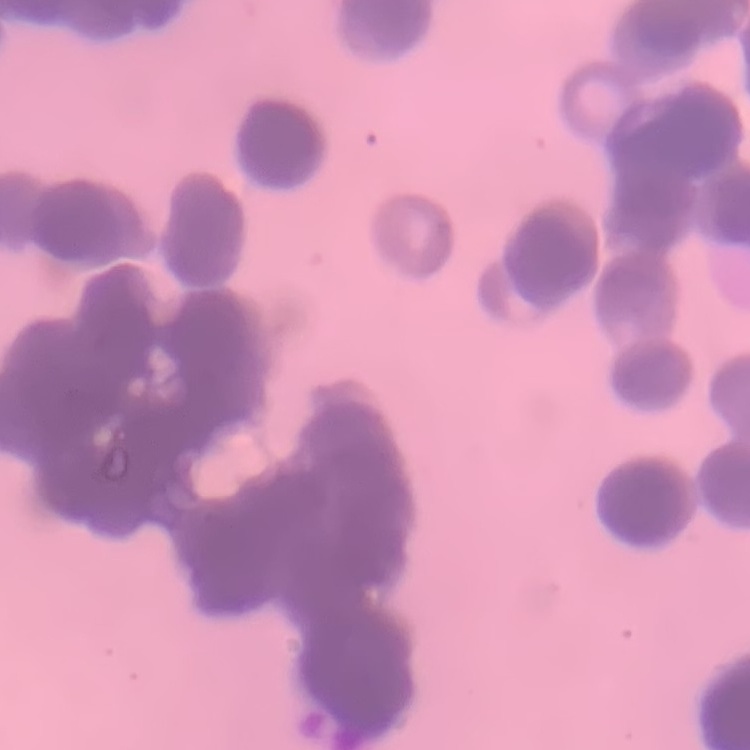
The red blood cells show rouleaux formation. Field's or Giemsa stain. Thin peripheral smear. One tile cut from a larger photomicrograph.